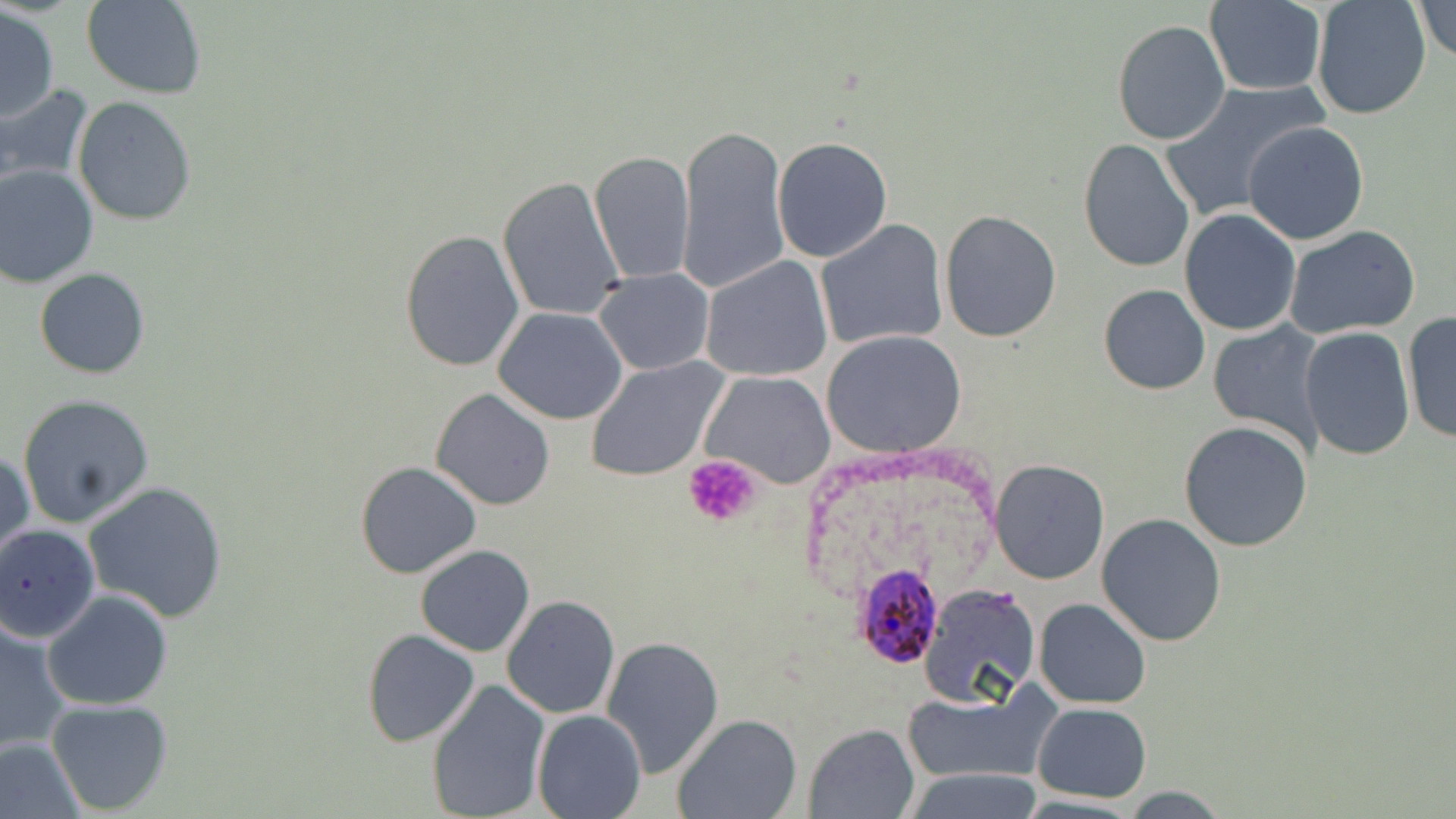
Summary:
  - Coordinate format: approximate bounding boxes as named x1/y1/x2/y2 corners in pixels
  - Platelet locations: (x1=684, y1=454, x2=763, y2=530)
  - Plasmodium ovale-infected red blood cell locations: (x1=852, y1=564, x2=944, y2=668)
  - Uninfected red blood cell locations: (x1=82, y1=0, x2=206, y2=98), (x1=1310, y1=0, x2=1433, y2=119), (x1=1412, y1=0, x2=1456, y2=63), (x1=1204, y1=1, x2=1326, y2=97), (x1=1, y1=7, x2=59, y2=123), (x1=1111, y1=19, x2=1231, y2=145), (x1=1160, y1=80, x2=1327, y2=220), (x1=0, y1=83, x2=95, y2=190), (x1=72, y1=96, x2=197, y2=225), (x1=1242, y1=120, x2=1369, y2=246), (x1=676, y1=123, x2=790, y2=296), (x1=771, y1=136, x2=893, y2=263), (x1=1078, y1=138, x2=1195, y2=271), (x1=589, y1=151, x2=696, y2=286), (x1=0, y1=165, x2=98, y2=287), (x1=497, y1=175, x2=626, y2=322), (x1=1179, y1=208, x2=1302, y2=335), (x1=939, y1=209, x2=1064, y2=342), (x1=816, y1=220, x2=948, y2=353), (x1=1284, y1=224, x2=1421, y2=339), (x1=399, y1=229, x2=526, y2=371), (x1=701, y1=256, x2=833, y2=381), (x1=34, y1=268, x2=152, y2=378), (x1=592, y1=268, x2=714, y2=376), (x1=1098, y1=284, x2=1212, y2=396), (x1=493, y1=308, x2=628, y2=424), (x1=1402, y1=311, x2=1456, y2=446), (x1=1205, y1=319, x2=1326, y2=456), (x1=1299, y1=328, x2=1416, y2=462), (x1=822, y1=331, x2=965, y2=456), (x1=585, y1=355, x2=730, y2=482), (x1=701, y1=371, x2=836, y2=488), (x1=431, y1=387, x2=555, y2=510), (x1=17, y1=394, x2=154, y2=526), (x1=1178, y1=421, x2=1314, y2=553), (x1=0, y1=449, x2=33, y2=562), (x1=989, y1=459, x2=1110, y2=585), (x1=356, y1=461, x2=482, y2=578), (x1=82, y1=481, x2=229, y2=623), (x1=1096, y1=514, x2=1227, y2=647), (x1=0, y1=523, x2=98, y2=646), (x1=414, y1=545, x2=536, y2=657), (x1=917, y1=584, x2=1040, y2=708), (x1=43, y1=591, x2=173, y2=710), (x1=501, y1=595, x2=620, y2=719), (x1=1034, y1=599, x2=1150, y2=709), (x1=1, y1=619, x2=72, y2=753), (x1=362, y1=628, x2=481, y2=748), (x1=602, y1=635, x2=725, y2=776), (x1=427, y1=679, x2=551, y2=819), (x1=902, y1=687, x2=1055, y2=785), (x1=46, y1=698, x2=174, y2=816), (x1=1032, y1=702, x2=1152, y2=802), (x1=531, y1=708, x2=647, y2=818), (x1=671, y1=712, x2=802, y2=819), (x1=804, y1=725, x2=918, y2=817), (x1=0, y1=735, x2=86, y2=819), (x1=901, y1=768, x2=1045, y2=818), (x1=1118, y1=787, x2=1232, y2=817)
  - Slide-level diagnosis: Plasmodium ovale
  - Modality: optical microscopy
  - Stain: May-Grünwald-Giemsa
  - Preparation: thin blood film
  - Image size: 1456×819 pixels
  - Magnification: 1000x
  - Field of view: single